Give the position of every Plasmodium parasite and every leukocyte.
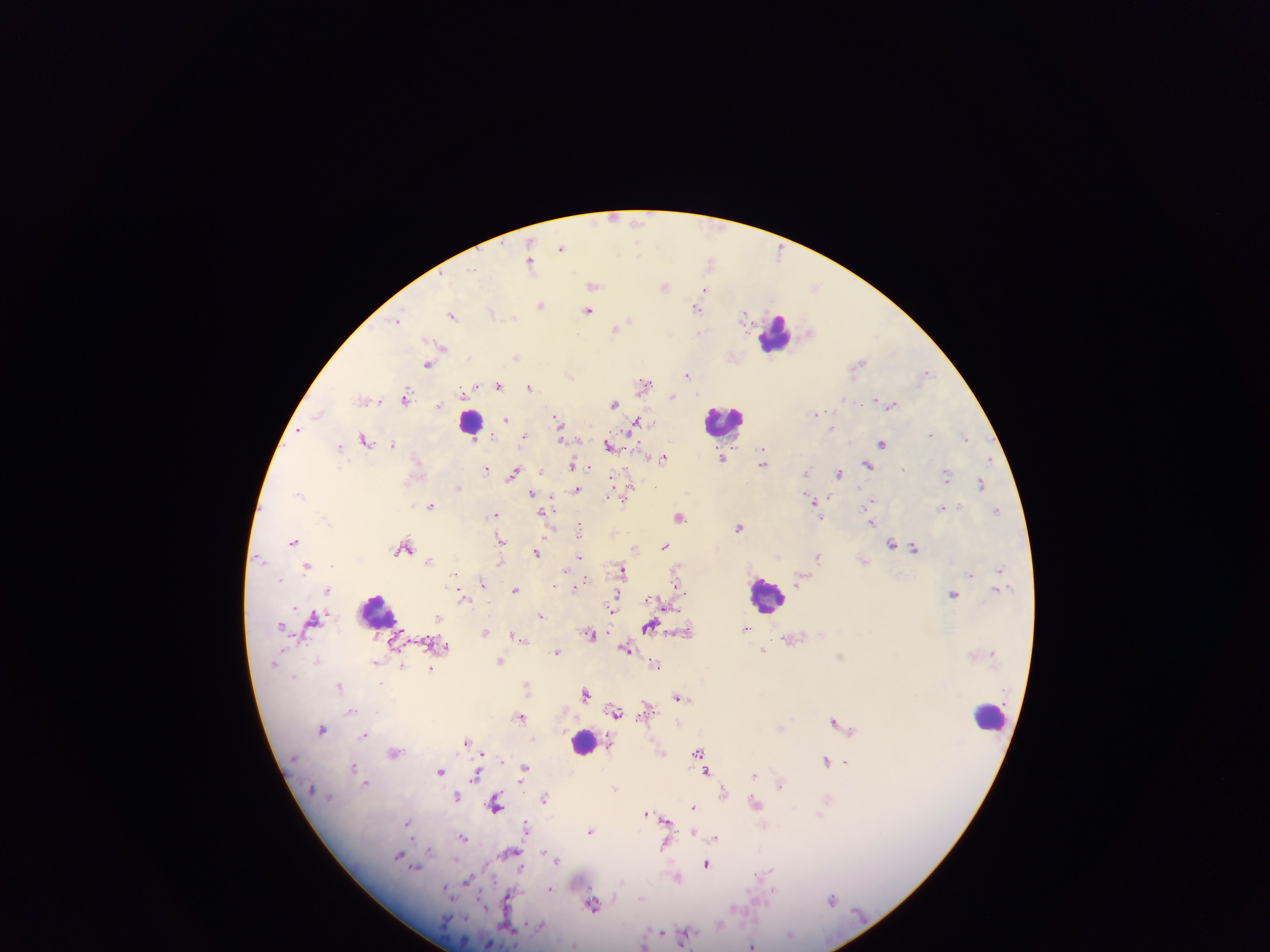

Approximate centers as (x, y) in pixels.
Plasmodium parasites: (614, 218), (639, 221), (562, 247), (638, 252), (710, 261), (531, 263), (472, 269), (594, 285), (665, 286), (816, 287), (704, 290), (540, 305), (697, 308), (588, 310), (491, 311), (453, 314), (745, 314), (514, 317), (397, 319), (628, 321), (615, 329), (699, 331), (809, 331), (439, 344), (516, 357), (858, 364), (427, 365), (689, 374), (925, 374), (570, 375), (644, 384), (499, 386), (530, 386), (463, 392), (673, 396), (407, 397), (363, 399), (614, 403), (439, 405), (891, 405), (318, 412), (816, 414), (507, 420), (558, 422), (636, 423), (832, 427), (299, 431), (930, 434), (525, 436), (966, 437), (366, 439), (882, 443), (393, 444), (610, 445), (340, 446), (645, 456), (663, 457), (722, 459), (763, 462), (573, 465), (586, 465), (868, 465), (486, 468), (903, 469), (806, 470), (838, 472), (514, 473), (946, 475), (613, 479), (981, 484), (628, 487), (458, 488), (577, 490), (300, 493), (532, 493), (626, 495), (824, 500), (813, 501), (871, 501), (430, 505), (942, 507), (997, 512), (543, 514), (494, 515), (679, 517), (821, 518), (871, 523), (739, 527), (580, 530), (293, 541), (501, 541), (891, 543), (665, 546), (404, 548), (914, 548), (634, 549), (536, 553), (818, 556), (579, 558), (429, 561), (500, 563), (307, 566), (999, 569), (622, 570), (971, 575), (800, 580), (483, 584), (677, 584), (554, 585), (575, 588), (515, 589), (328, 591), (953, 594), (616, 597), (461, 598), (541, 616), (438, 617), (313, 620), (282, 624), (650, 625), (745, 630), (486, 632), (682, 632), (514, 634), (590, 634), (626, 648), (764, 650), (557, 652), (317, 661), (501, 661), (655, 664), (402, 665), (430, 669), (340, 686), (526, 686), (586, 693), (678, 698), (647, 708), (352, 711), (617, 712), (521, 717), (835, 720), (322, 728), (781, 728), (365, 735), (467, 741), (698, 751), (394, 752), (662, 753), (826, 759), (847, 762), (354, 767), (524, 769), (440, 771), (706, 772), (476, 775), (754, 775), (366, 782), (781, 783), (615, 788), (724, 790), (457, 796), (545, 798), (496, 804), (756, 804), (694, 807), (647, 813), (664, 820), (408, 824), (526, 826), (590, 830), (693, 831), (697, 834), (463, 837), (715, 838), (664, 844), (429, 849), (511, 853), (548, 853), (399, 854), (552, 856), (557, 860), (706, 863), (416, 869), (763, 876), (677, 877), (468, 881), (550, 888), (774, 893), (510, 897), (832, 899), (593, 905), (661, 931), (685, 935), (752, 945).
Leukocytes: (777, 333), (724, 421), (472, 422), (766, 595), (377, 613), (990, 715), (583, 740).

field of view = single
country = Ghana
capture = mobile-phone photograph through a microscope
image size = 1270×952 pixels
preparation = thick blood film